Assess the morphology of the red blood cells.
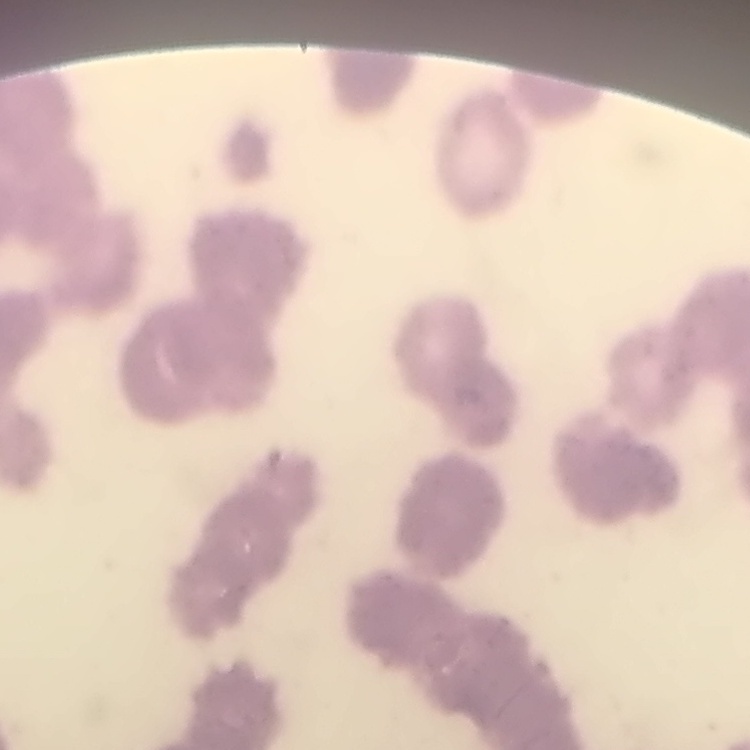
Rouleaux formation.

{
  "stain": "Field's or Giemsa",
  "image_type": "square crop of a larger photomicrograph",
  "preparation": "thin blood film"
}